Assess the morphology of the erythrocytes.
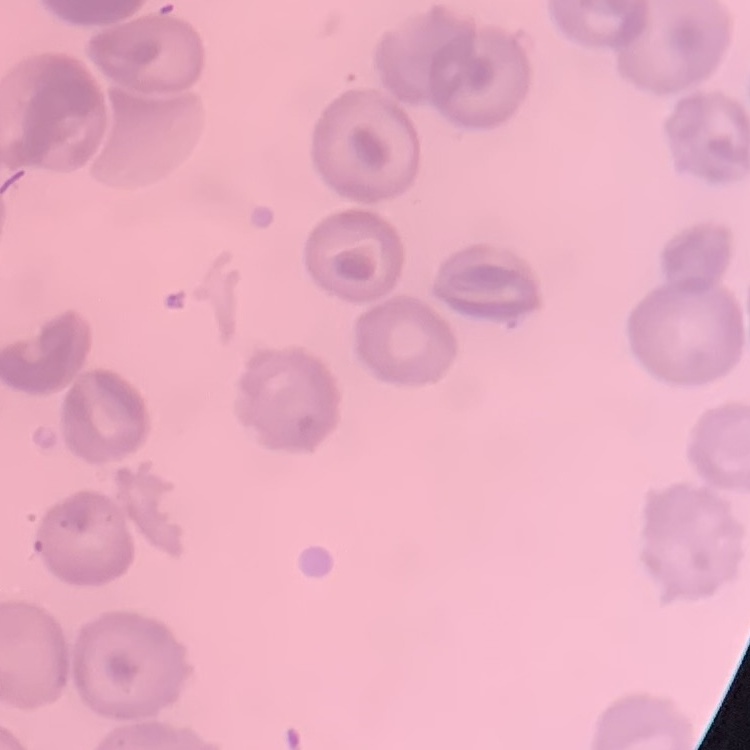

They show no rouleaux formation.

image type = square crop of a larger photomicrograph
preparation = thin blood smear
stain = Field's or Giemsa